Assess this cell for malaria.
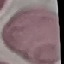

It is uninfected.

Photographed with a smartphone camera at the microscope eyepiece. Cell patch, automatically extracted from a larger field of view and resized to 64 × 64 pixels. Thin blood smear. Giemsa-stained preparation.